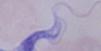
Summary:
  - Identification: trypanosome
  - Magnification: 1000x
  - Modality: micrograph